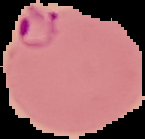

From a thin blood smear. Image is 145×139 pixels. Malaria status: parasitized. Segmented cell region on a black background.